Give the position of every malaria parasite.
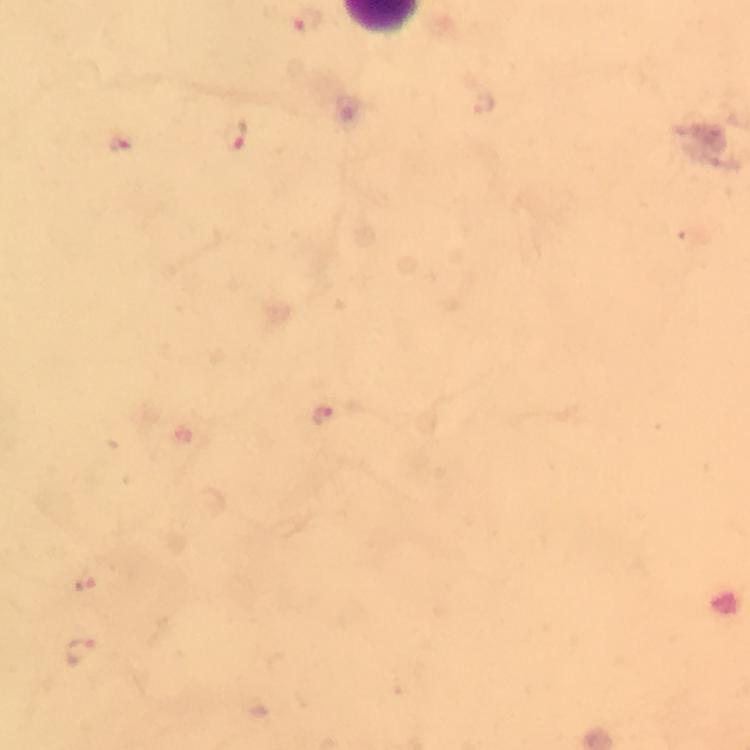

Approximate centers as [x, y] in pixels.
Malaria parasites: [305, 22], [237, 138], [121, 141], [324, 416], [86, 581], [83, 652].

Summary:
  - Preparation: thick blood smear
  - Context: from a diagnostic examination for malaria
  - Immersion oil: applied
  - Image size: 750×750 pixels
  - Cropped from: one field of view
  - Stain: Giemsa
  - Capture: smartphone camera through the microscope
  - Magnification: 100x